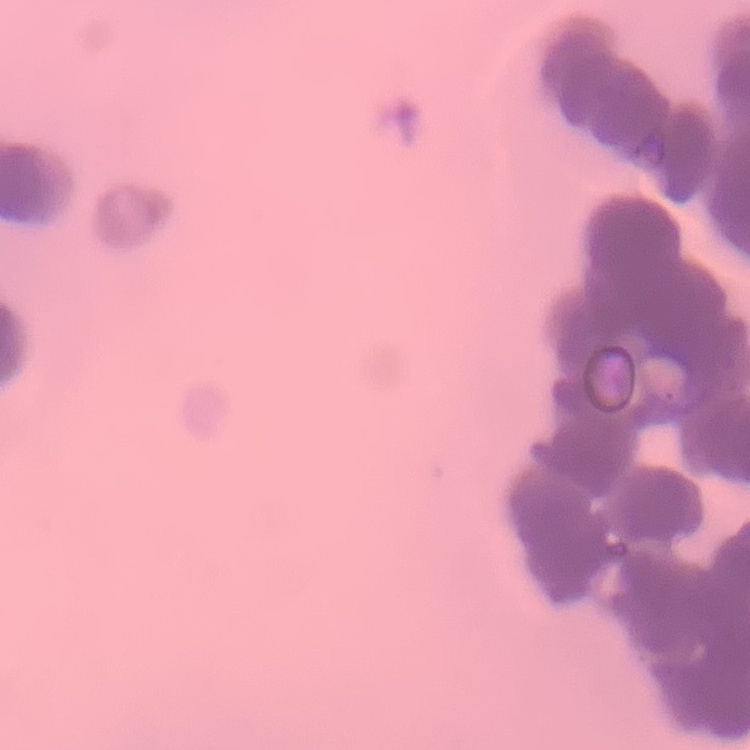

{
  "erythrocyte_morphology": "rouleaux formation",
  "preparation": "thin blood film",
  "stain": "Field's or Giemsa",
  "image_type": "square crop of a larger photomicrograph"
}